Name the cell type shown.
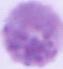
This is an erythrocyte.

Micrograph. Captured at 1000x magnification.